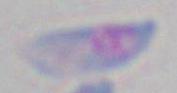 Captured at 1000x magnification. Toxoplasma gondii is seen. Photomicrograph.